Point out each Plasmodium parasite.
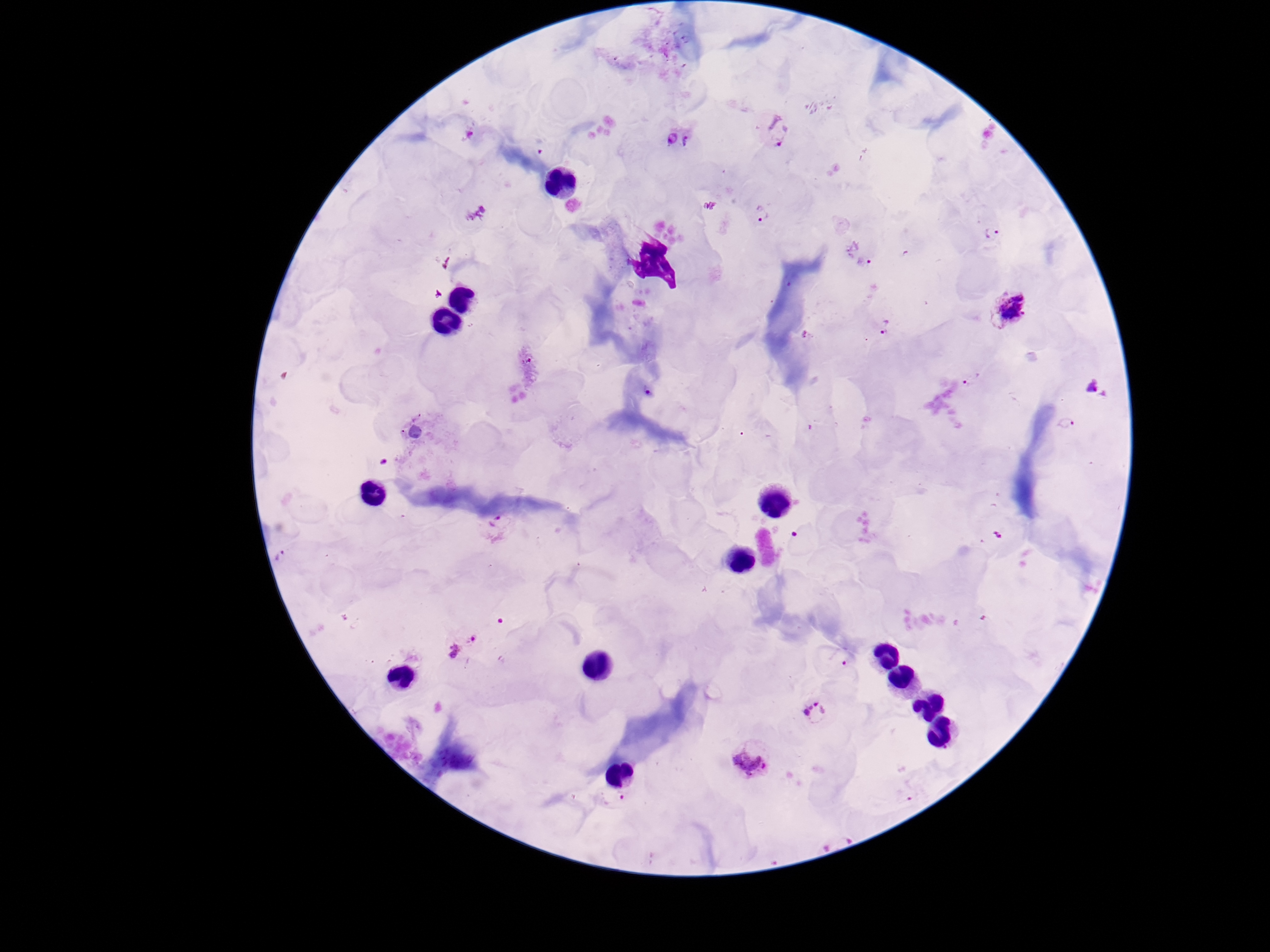

Approximate centers as [x, y] in pixels.
Plasmodium parasites: [775, 128], [467, 131], [671, 137], [686, 138], [761, 212], [992, 231], [865, 262], [1009, 307], [883, 327], [970, 380], [1093, 387], [648, 389], [1066, 422], [494, 520], [1000, 534], [460, 643], [844, 663], [816, 712], [749, 761], [622, 794].

magnification = 100x
image size = 1270×952 pixels
capture = smartphone camera through the microscope eyepiece
preparation = thick peripheral-blood smear
patient malaria status = positive
stain = Giemsa
field of view = single